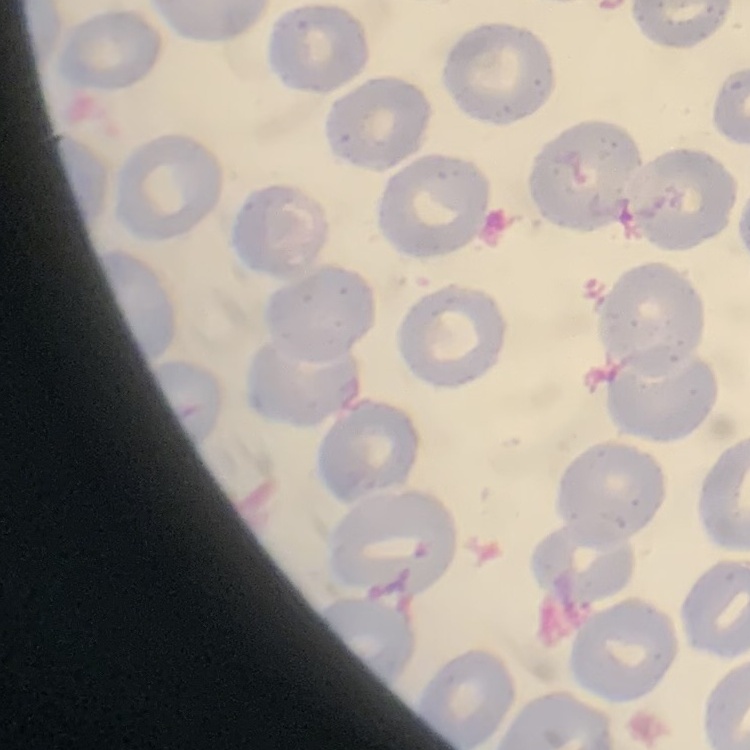
The red blood cells show no rouleaux formation. Thin blood film. Square crop of a larger photomicrograph. Stained with either Field's or Giemsa.